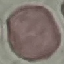
Summary:
  - Result: no malaria parasites seen
  - Stain: Giemsa
  - Image type: cell patch, automatically extracted from a larger field of view and resized to 64 × 64 pixels
  - Preparation: thin smear
  - Capture: smartphone camera at the microscope eyepiece